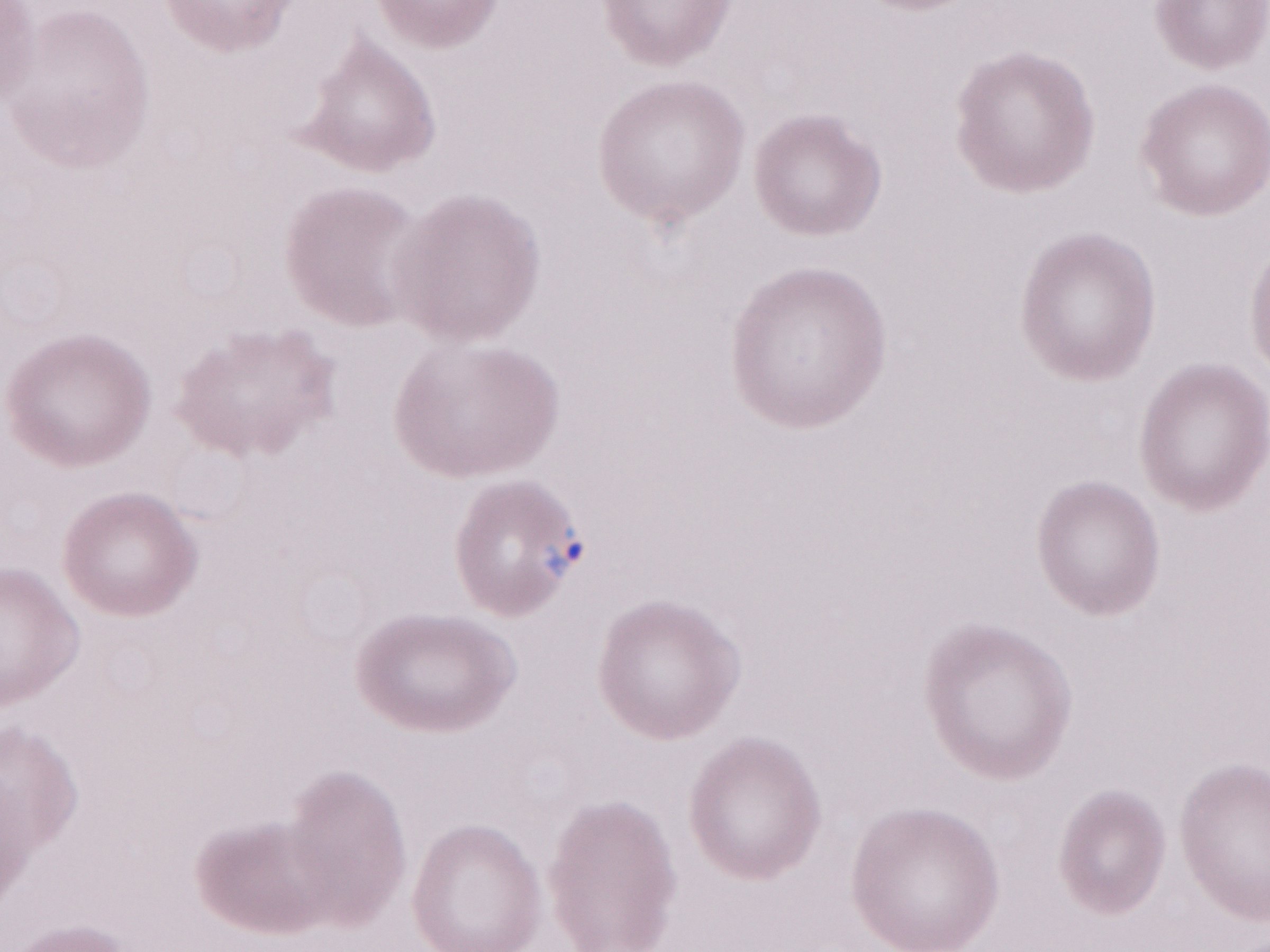

Thin blood film. Image is 1270×952 pixels. Patient diagnosis: malaria infection. One field of this slide. Olympus BX43 microscope, Olympus DP73 camera. 1,000x magnification. May-Grünwald-Giemsa (MGG) stain.